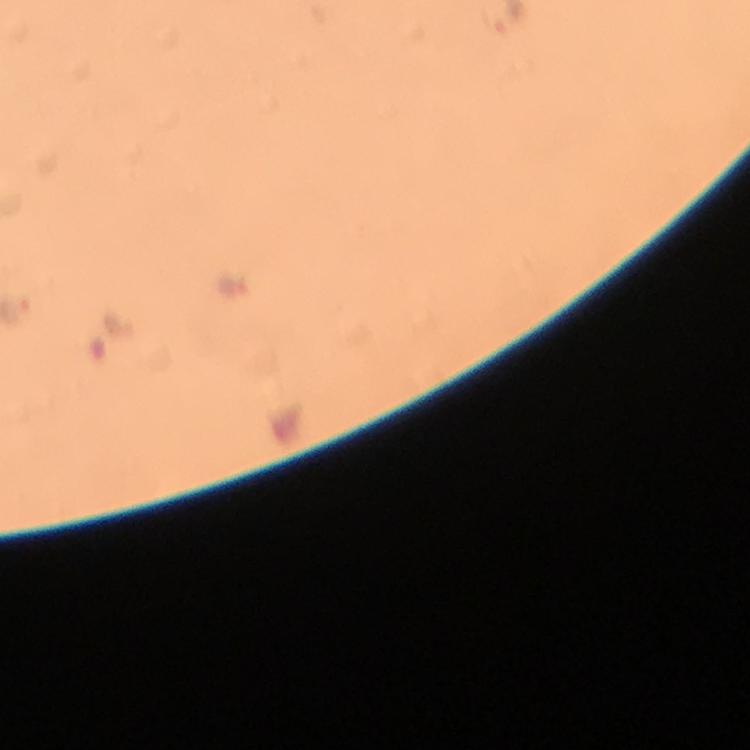
stain = Giemsa
context = from a diagnostic examination for malaria
preparation = thick blood film
image size = 750×750 pixels
malaria parasite locations = approximate centers as (x, y) in pixels: (234, 288)
immersion oil = applied
magnification = 100x
capture = smartphone photograph through a microscope
cropped from = one field of view